Classify this cell by malaria status.
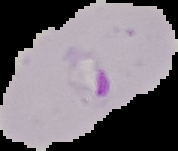

It is parasitized.

The area outside the segmented cell region is set to black. From a thin blood smear. Image is 178×151 pixels.